Locate every uninfected red blood cell.
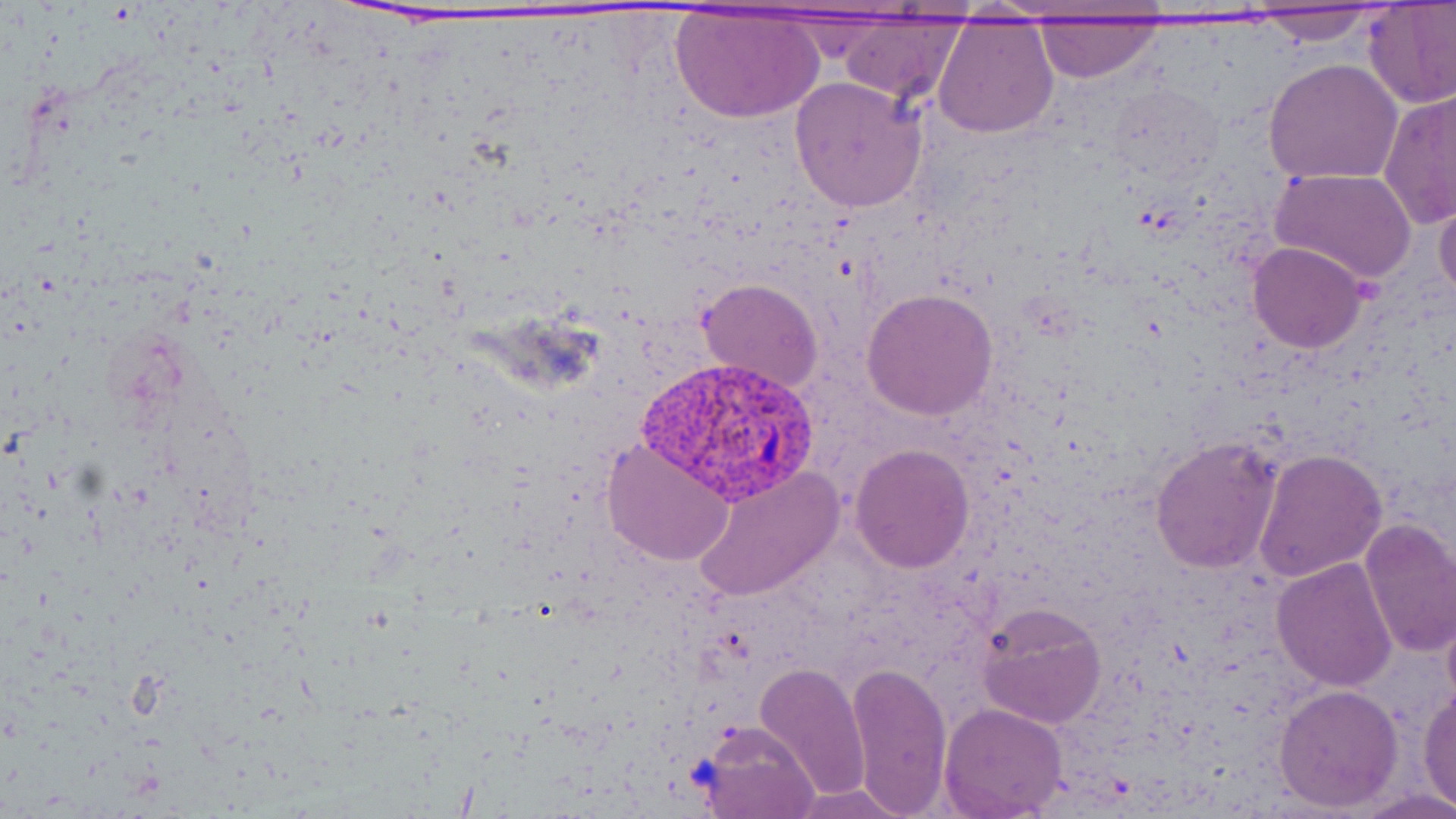

Approximate bounding boxes as (x1,y1)-(x2,y2) corner pairs in pixels.
Uninfected red blood cells: (1363,3)-(1456,109), (1242,7)-(1392,43), (669,8)-(823,124), (832,15)-(968,104), (932,17)-(1059,138), (1030,17)-(1162,82), (1263,58)-(1404,186), (789,75)-(929,214), (1106,83)-(1225,184), (1380,89)-(1456,230), (1270,167)-(1418,285), (1433,189)-(1456,304), (1248,242)-(1367,353), (697,279)-(822,392), (860,289)-(999,420), (1150,435)-(1285,573), (602,438)-(734,568), (851,444)-(975,573), (1253,447)-(1387,583), (691,465)-(841,602), (1357,518)-(1456,657), (1270,556)-(1399,692), (1441,601)-(1456,718), (976,602)-(1106,729), (845,661)-(952,814), (753,662)-(870,798), (1273,684)-(1402,811), (1418,687)-(1456,808), (938,703)-(1068,817), (698,720)-(820,819), (787,784)-(913,817).

plasmodium_vivax_infected_red_blood_cell_locations: 'approximate bounding boxes as (x1,y1)-(x2,y2) corner pairs in pixels: (641,354)-(818,501)'
slide_level_diagnosis: Plasmodium vivax
preparation: thin blood smear
stain: May-Grünwald-Giemsa
magnification: 1000x
field_of_view: single
modality: optical microscopy
image_size: 1456×819 pixels